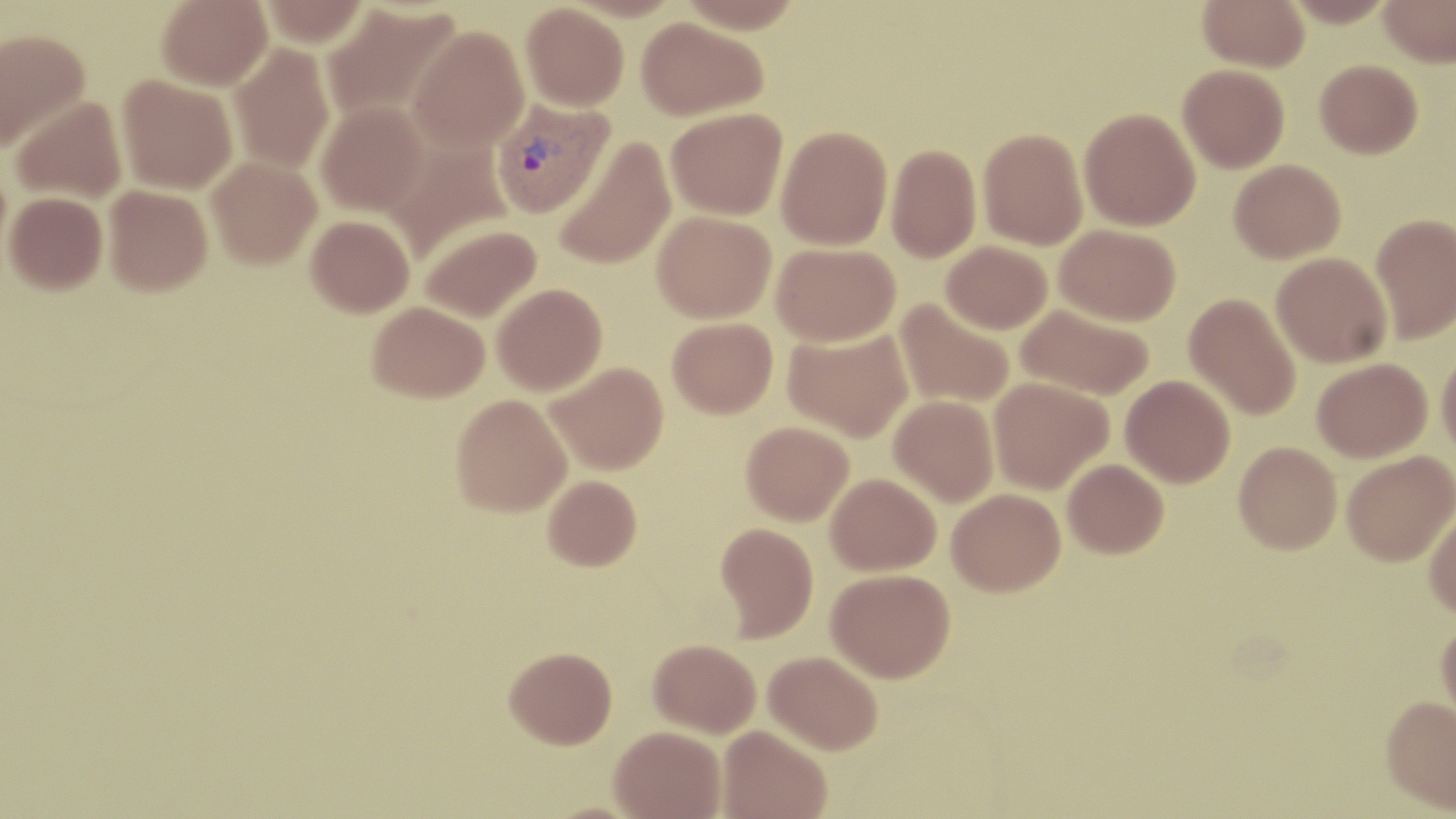
Summary:
  - Coordinate format: approximate bounding boxes as (x1, y1, x2, y2) in pixels
  - Plasmodium vivax-infected red blood cell locations: (490, 98, 613, 219)
  - Uninfected red blood cell locations: (156, 0, 272, 90), (260, 0, 371, 46), (677, 0, 805, 33), (1198, 0, 1309, 71), (1282, 0, 1398, 26), (1378, 0, 1456, 67), (321, 2, 462, 125), (521, 3, 629, 111), (636, 17, 768, 121), (407, 25, 529, 155), (0, 29, 90, 152), (230, 43, 336, 174), (1315, 60, 1423, 158), (1178, 64, 1289, 173), (117, 74, 237, 194), (10, 97, 127, 203), (316, 101, 429, 216), (666, 107, 788, 220), (1079, 107, 1201, 231), (776, 124, 893, 250), (978, 127, 1088, 249), (554, 137, 676, 271), (383, 138, 512, 264), (886, 143, 981, 262), (207, 156, 321, 269), (1229, 159, 1346, 263), (103, 185, 212, 296), (4, 192, 107, 296), (652, 211, 776, 323), (1370, 212, 1456, 343), (306, 215, 414, 317), (419, 223, 541, 323), (1055, 224, 1181, 326), (941, 240, 1052, 334), (771, 242, 900, 347), (1272, 252, 1392, 367), (492, 283, 607, 396), (1184, 293, 1302, 421), (895, 300, 1014, 409), (367, 301, 489, 402), (1016, 303, 1155, 400), (667, 318, 778, 418), (783, 328, 913, 442), (1437, 347, 1456, 460), (1313, 357, 1432, 462), (546, 361, 669, 475), (1121, 375, 1235, 487), (988, 378, 1113, 494), (450, 394, 572, 517), (889, 395, 999, 506), (741, 421, 854, 525), (1234, 441, 1342, 554), (1342, 451, 1455, 566), (1063, 458, 1169, 558), (825, 473, 941, 576), (543, 475, 642, 571), (947, 488, 1066, 596), (1425, 509, 1456, 619), (715, 522, 818, 642), (826, 569, 955, 683), (1436, 617, 1456, 728), (648, 639, 760, 737), (504, 646, 617, 749), (764, 650, 883, 754), (1380, 696, 1456, 813), (718, 725, 832, 819), (610, 726, 726, 819)
  - Slide-level diagnosis: Plasmodium vivax
  - Field of view: one of a larger specimen
  - Image size: 1456×819 pixels
  - Modality: optical microscopy
  - Magnification: 1000x
  - Preparation: thin blood smear
  - Stain: May-Grünwald-Giemsa